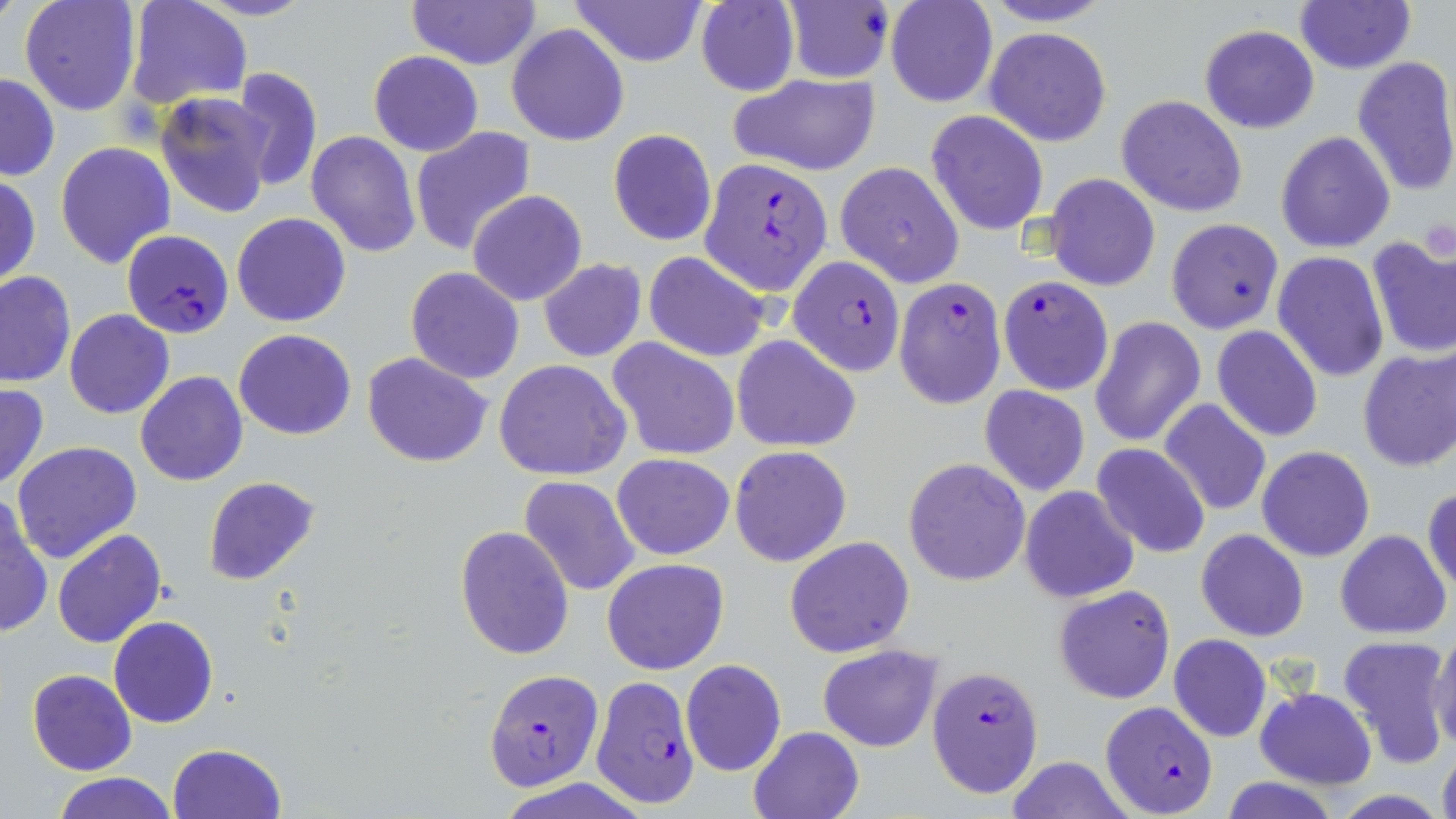 Approximate bounding boxes as (x1, y1, x2, y2) in pixels. Plasmodium falciparum-infected red blood cell locations: (702, 158, 832, 295), (122, 230, 233, 338), (788, 254, 907, 375), (997, 275, 1111, 405), (893, 278, 1002, 406), (483, 667, 604, 790), (927, 667, 1044, 800), (593, 679, 700, 805), (1099, 700, 1219, 818). Uninfected red blood cell locations: (19, 0, 143, 117), (124, 0, 253, 113), (406, 0, 542, 69), (567, 0, 707, 66), (978, 0, 1121, 26), (782, 1, 893, 84), (884, 1, 998, 108), (1295, 1, 1415, 75), (694, 2, 799, 95), (506, 23, 630, 147), (1199, 25, 1319, 134), (984, 27, 1112, 147), (369, 50, 484, 157), (1352, 55, 1456, 195), (230, 68, 322, 192), (729, 71, 881, 177), (1, 72, 60, 181), (156, 91, 273, 218), (1117, 94, 1246, 217), (926, 110, 1049, 236), (410, 125, 535, 256), (608, 128, 716, 247), (305, 130, 420, 258), (1276, 131, 1395, 253), (54, 140, 176, 268), (835, 162, 965, 286), (1045, 173, 1160, 291), (0, 176, 42, 288), (468, 190, 587, 307), (231, 212, 352, 327), (1165, 218, 1283, 334), (1366, 238, 1456, 359), (644, 251, 769, 361), (1272, 252, 1389, 383), (538, 259, 646, 362), (406, 266, 525, 384), (0, 270, 75, 388), (65, 310, 175, 419), (1090, 316, 1207, 447), (1212, 326, 1323, 442), (233, 329, 357, 440), (731, 335, 861, 453), (608, 339, 741, 460), (1357, 346, 1456, 472), (362, 353, 493, 468), (495, 358, 631, 481), (136, 372, 247, 487), (0, 382, 49, 491), (979, 385, 1090, 495), (1157, 398, 1272, 518), (11, 441, 142, 565), (1092, 444, 1211, 558), (729, 446, 852, 567), (1257, 446, 1374, 562), (612, 453, 735, 560), (904, 457, 1031, 586), (518, 475, 643, 598), (202, 476, 322, 588), (1019, 485, 1140, 604), (1424, 486, 1456, 598), (0, 499, 52, 638), (454, 524, 574, 661), (51, 528, 166, 649), (1196, 529, 1308, 642), (1336, 530, 1450, 639), (784, 535, 915, 658), (601, 558, 730, 675), (1054, 585, 1176, 705), (108, 616, 219, 728), (1430, 626, 1456, 754), (1169, 634, 1271, 742), (1336, 634, 1452, 766), (817, 643, 945, 752), (681, 659, 786, 777), (27, 669, 136, 775), (1255, 687, 1377, 788), (746, 725, 865, 819), (167, 743, 287, 819), (1437, 743, 1456, 819), (1004, 756, 1136, 819), (53, 773, 179, 819), (1221, 777, 1340, 819). Slide-level diagnosis: Plasmodium falciparum. Thin blood smear. One field of a larger specimen. Image is 1456×819 pixels. Optical microscopy. Captured at 1000x magnification. May-Grünwald-Giemsa stain.